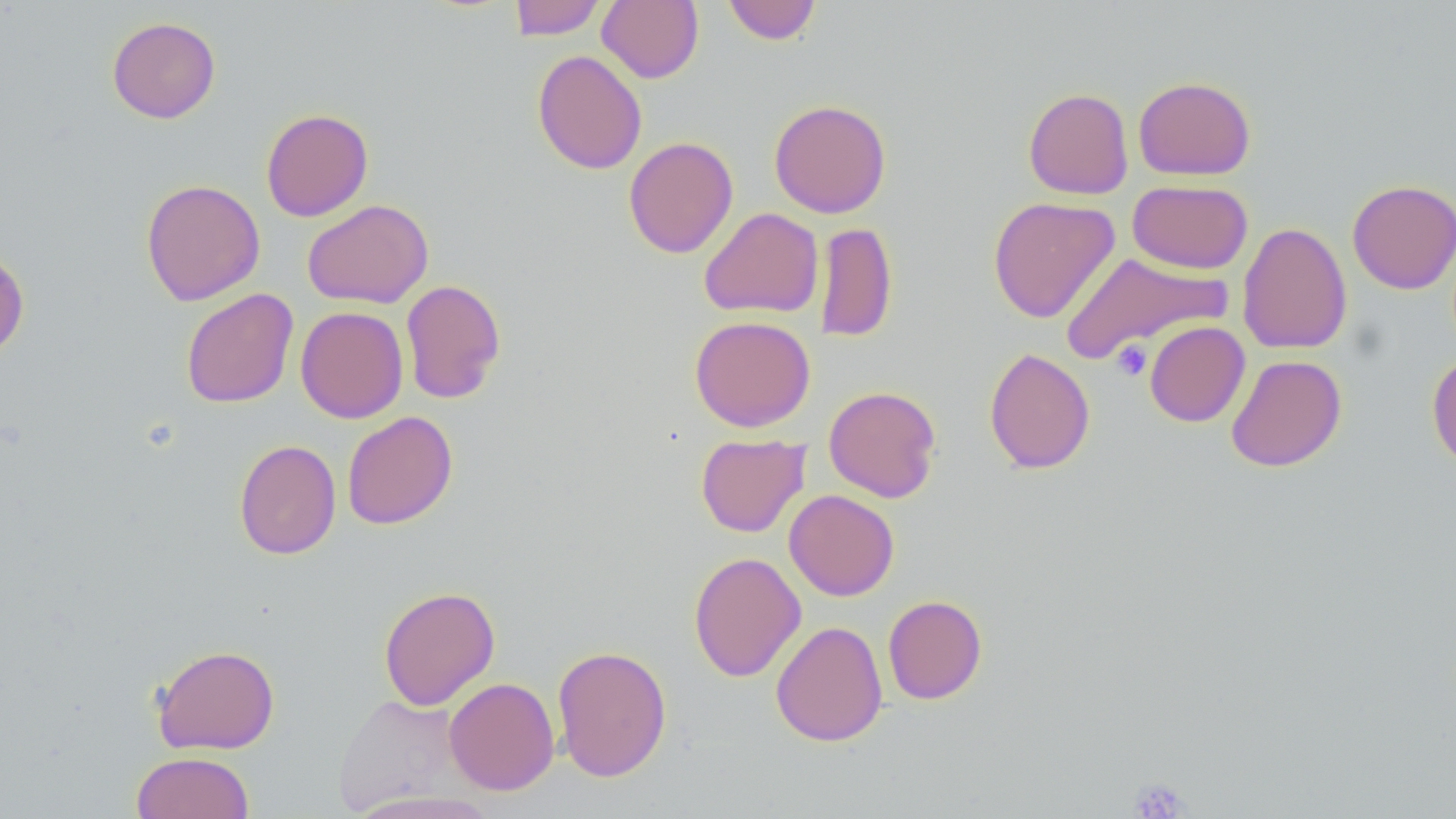
Summary:
  - Coordinate format: approximate bounding boxes as (x1, y1, x2, y2) in pixels
  - Platelet locations: (1111, 341, 1153, 380), (1127, 777, 1192, 817)
  - Uninfected red blood cell locations: (508, 0, 607, 40), (597, 0, 704, 84), (722, 0, 822, 45), (107, 16, 221, 124), (532, 50, 647, 175), (1133, 76, 1256, 180), (1023, 87, 1134, 200), (769, 99, 891, 218), (260, 108, 374, 222), (623, 137, 739, 258), (140, 179, 266, 306), (1346, 179, 1456, 294), (1127, 180, 1253, 274), (987, 196, 1120, 323), (302, 199, 433, 309), (699, 207, 824, 319), (815, 222, 897, 343), (1237, 222, 1353, 355), (0, 247, 30, 361), (1061, 252, 1231, 363), (399, 279, 506, 404), (180, 288, 299, 408), (295, 306, 409, 423), (689, 315, 816, 432), (1144, 321, 1250, 427), (983, 347, 1096, 474), (1427, 353, 1456, 472), (1226, 355, 1347, 472), (823, 385, 943, 503), (341, 411, 457, 530), (695, 433, 809, 537), (234, 439, 341, 560), (784, 489, 899, 601), (688, 551, 806, 682), (378, 585, 500, 710), (882, 595, 987, 705), (770, 620, 888, 747), (151, 643, 280, 754), (552, 644, 672, 783), (443, 677, 560, 796), (333, 693, 465, 813), (131, 751, 255, 819), (345, 790, 502, 819)
  - Slide-level diagnosis: no evidence of blood parasites
  - Stain: May-Grünwald-Giemsa
  - Field of view: one of a larger specimen
  - Modality: light microscopy
  - Magnification: 1000x
  - Image size: 1456×819 pixels
  - Preparation: thin blood smear